Name the parasite shown.
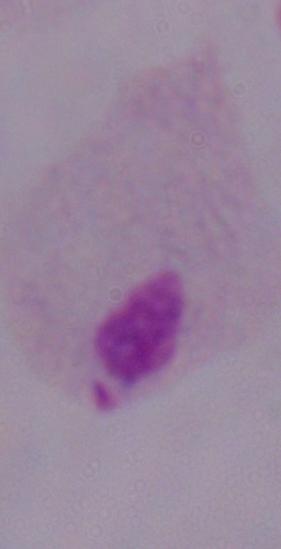
A trichomonad.

Photomicrograph. 1000x magnification.